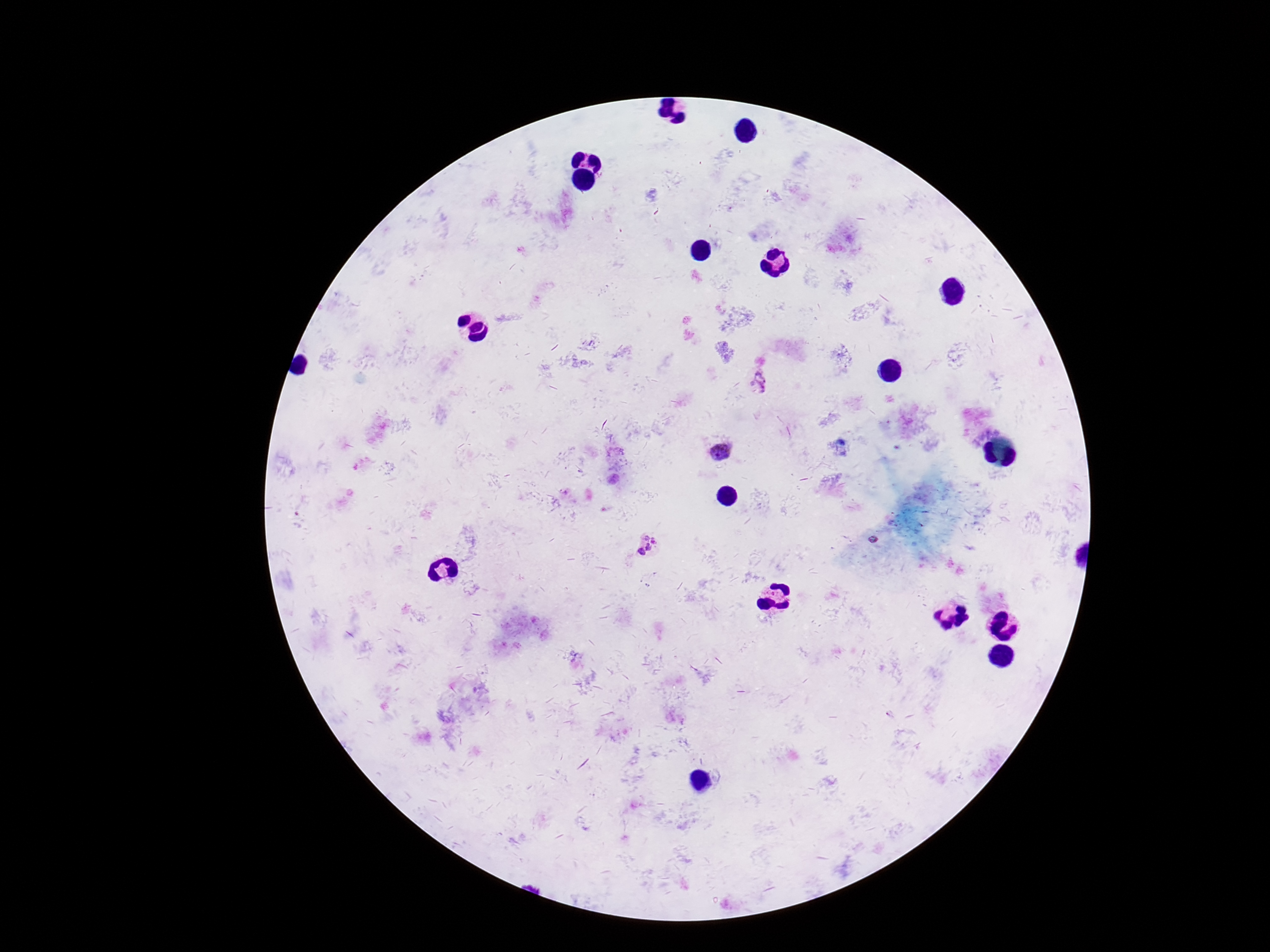
image size = 1270×952 pixels
patient malaria status = infected
field of view = single
preparation = thick blood film
Plasmodium parasite locations = approximate centers as [x, y] in pixels: [759, 384], [720, 452], [873, 540], [649, 547]
stain = Giemsa
magnification = 100x
capture = smartphone camera through the microscope eyepiece